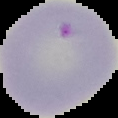
Image is 118×118 pixels. From a thin blood film. Result: malaria parasites detected. Segmented cell region on a black background.